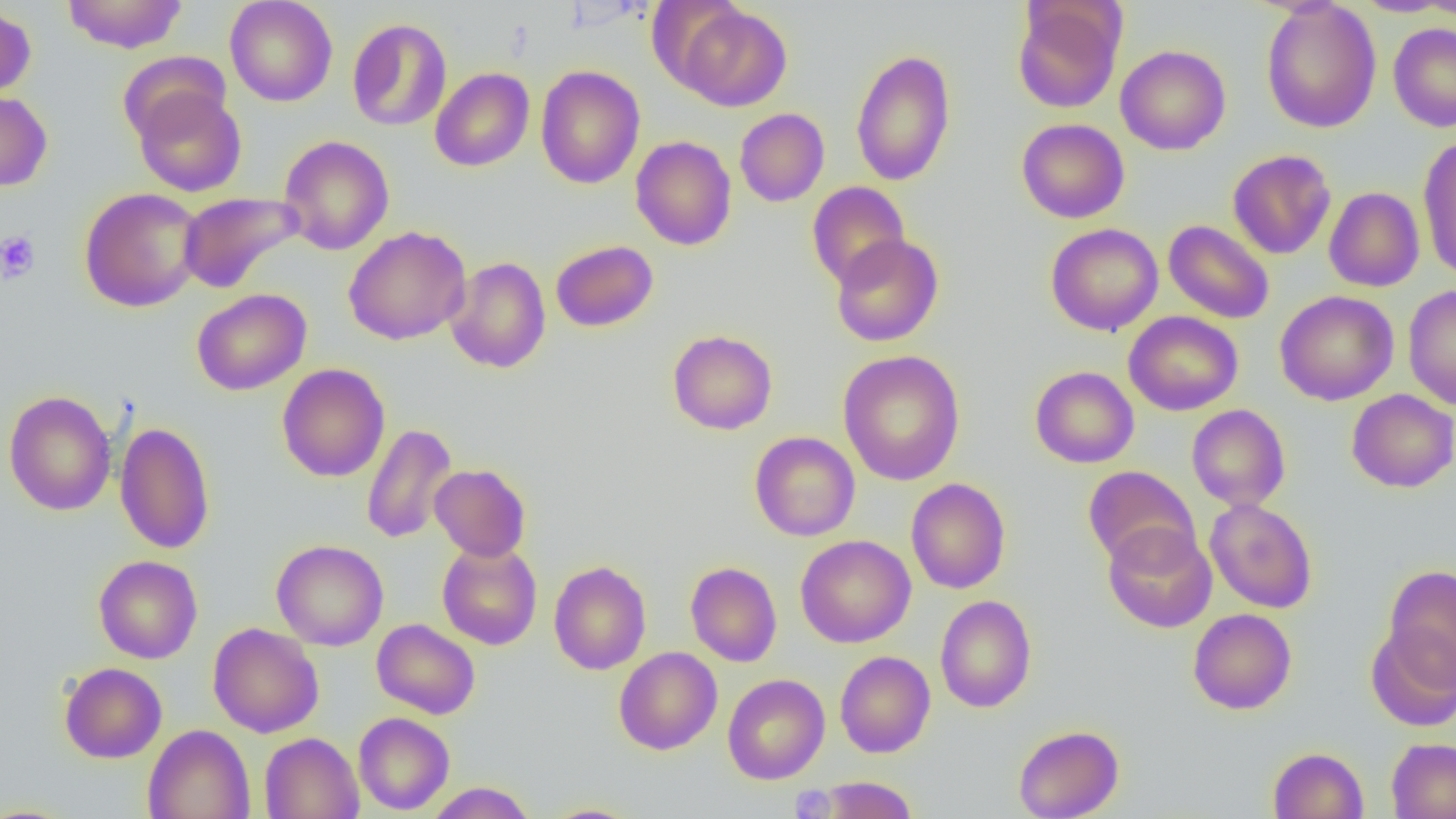
{
  "slide_level_diagnosis": "no evidence of blood parasites",
  "image_size": "1456×819 pixels",
  "preparation": "thin blood film",
  "field_of_view": "one of a larger specimen",
  "magnification": "1000x",
  "platelet_locations": "approximate bounding boxes as [x1, y1, x2, y2] in pixels: [0, 230, 41, 283]",
  "modality": "light microscopy",
  "uninfected_red_blood_cell_locations": "approximate bounding boxes as [x1, y1, x2, y2] in pixels: [63, 0, 187, 53], [224, 0, 337, 106], [1011, 1, 1126, 113], [1261, 1, 1381, 133], [1350, 1, 1455, 17], [0, 4, 36, 100], [676, 4, 791, 111], [347, 18, 452, 131], [1388, 23, 1456, 133], [1116, 45, 1231, 155], [850, 48, 956, 186], [117, 50, 230, 143], [535, 66, 645, 189], [430, 67, 534, 171], [133, 87, 246, 197], [0, 90, 53, 191], [734, 108, 829, 207], [1016, 118, 1129, 223], [278, 135, 394, 255], [1417, 135, 1456, 280], [630, 136, 737, 250], [1227, 149, 1336, 259], [807, 181, 910, 288], [79, 187, 204, 312], [1324, 187, 1425, 292], [177, 191, 303, 293], [1163, 220, 1274, 324], [1046, 223, 1163, 335], [343, 226, 471, 345], [830, 234, 944, 347], [550, 240, 658, 332], [445, 257, 551, 374], [1403, 285, 1456, 410], [191, 288, 311, 395], [1275, 290, 1399, 406], [1123, 311, 1243, 416], [667, 329, 778, 435], [838, 350, 965, 485], [277, 363, 390, 482], [1030, 366, 1139, 468], [1346, 389, 1456, 493], [3, 391, 117, 516], [1186, 404, 1291, 512], [114, 421, 215, 554], [361, 423, 457, 544], [749, 431, 860, 541], [429, 464, 531, 561], [1083, 465, 1199, 569], [906, 478, 1011, 594], [1205, 498, 1318, 613], [1102, 523, 1217, 633], [795, 534, 916, 647], [271, 539, 389, 651], [437, 541, 542, 650], [436, 550, 651, 657], [93, 555, 202, 663], [549, 560, 651, 674], [685, 561, 782, 667], [1383, 564, 1456, 686], [935, 595, 1036, 712], [1188, 608, 1297, 714], [372, 619, 480, 719], [208, 623, 323, 737], [1365, 624, 1456, 732], [614, 647, 722, 755], [835, 651, 935, 758], [59, 661, 167, 763], [722, 673, 830, 784], [353, 712, 455, 814], [142, 724, 255, 819], [1013, 724, 1124, 819], [260, 732, 363, 819], [1386, 737, 1456, 818], [1268, 747, 1368, 819], [817, 776, 918, 818], [425, 782, 536, 818], [540, 803, 645, 819]"
}